Report the malaria status of this cell.
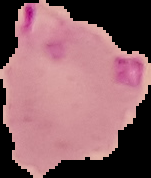

It is parasitized.

Summary:
  - Preparation: thin blood smear
  - Image size: 151×178 pixels
  - Image type: cell region segmented out of the field of view; surrounding area masked to black